State which cell type is depicted.
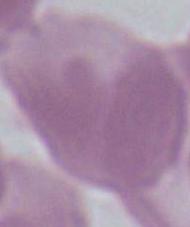
An erythrocyte.

Micrograph. 1000x magnification.